Classify this cell by malaria status.
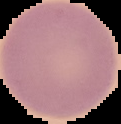
Uninfected.

Summary:
  - Image size: 121×124 pixels
  - Preparation: thin blood film
  - Image type: segmented cell region on a black background